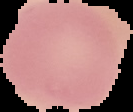
{
  "preparation": "thin blood film",
  "image_size": "133×112 pixels",
  "malaria_status": "uninfected",
  "image_type": "cell region segmented out of the field of view; surrounding area masked to black"
}